Report the malaria status of this cell.
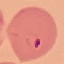
Parasitized.

Cell patch, automatically extracted from a larger field of view and resized to 64 × 64 pixels. Giemsa-stained preparation. Thin blood film. Acquired by smartphone through the microscope eyepiece.